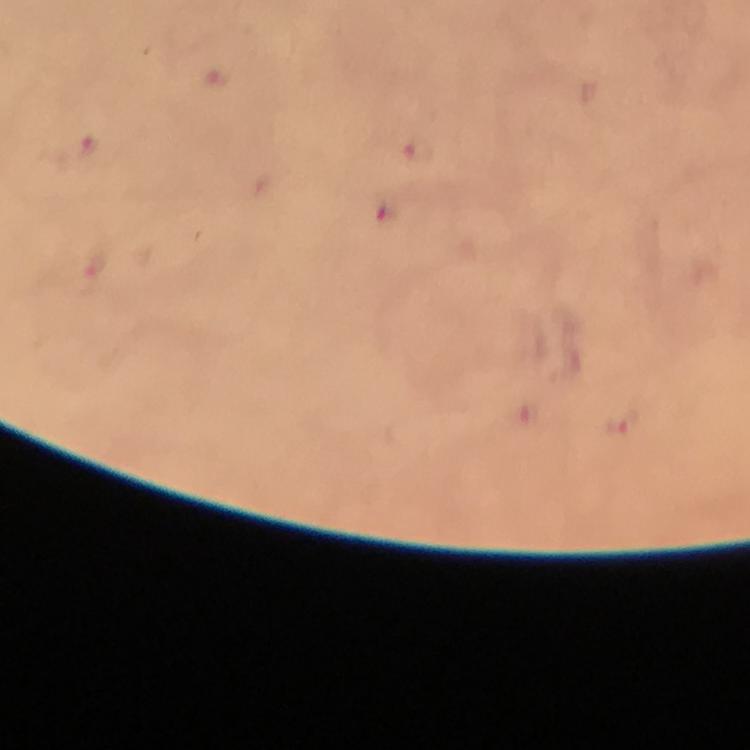
{
  "cropped_from": "one field of view",
  "plasmodium_parasite_locations": "approximate object centers, in pixels from the top-left corner: (x=88, y=146), (x=418, y=153), (x=621, y=424)",
  "immersion_oil": "used",
  "image_size": "750×750 pixels",
  "stain": "Giemsa",
  "magnification": "100x",
  "preparation": "thick smear",
  "context": "from a diagnostic examination for malaria",
  "capture": "smartphone photograph through a microscope"
}